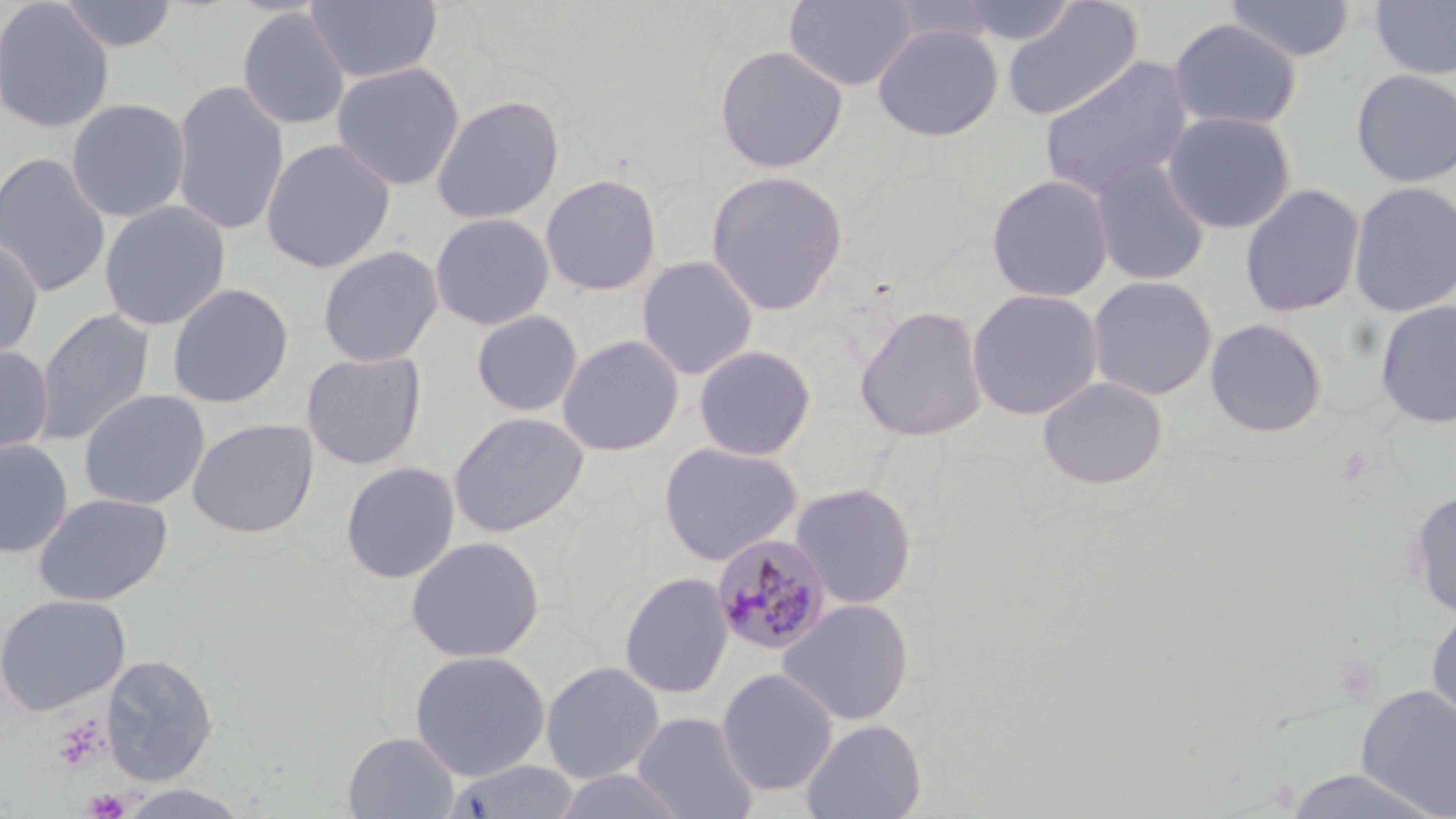
{
  "slide_level_diagnosis": "Plasmodium malariae",
  "preparation": "thin blood smear",
  "modality": "light microscopy",
  "field_of_view": "one of a larger specimen",
  "image_size": "1456×819 pixels",
  "uninfected_red_blood_cell_locations": "approximate bounding boxes as (x1, y1, x2, y2) in pixels: (0, 0, 115, 133), (56, 0, 181, 53), (305, 0, 443, 84), (784, 0, 918, 92), (952, 0, 1080, 46), (1001, 0, 1144, 121), (1223, 0, 1357, 62), (1370, 0, 1456, 79), (237, 7, 351, 131), (1167, 18, 1303, 132), (872, 23, 1004, 142), (713, 44, 849, 174), (1038, 55, 1194, 200), (331, 61, 466, 191), (1351, 68, 1456, 188), (171, 79, 290, 237), (431, 93, 565, 225), (66, 98, 191, 222), (1162, 110, 1297, 234), (260, 138, 397, 273), (0, 151, 112, 298), (1089, 156, 1212, 286), (705, 170, 850, 316), (540, 173, 663, 297), (986, 173, 1114, 303), (1348, 180, 1456, 318), (1240, 183, 1366, 318), (98, 199, 232, 331), (429, 212, 556, 331), (0, 234, 45, 363), (317, 245, 444, 367), (636, 255, 759, 379), (1087, 275, 1218, 401), (166, 282, 295, 409), (966, 287, 1104, 420), (1374, 300, 1456, 429), (853, 304, 989, 442), (34, 308, 155, 445), (470, 309, 584, 417), (1205, 318, 1328, 438), (556, 334, 685, 456), (692, 344, 818, 462), (0, 345, 54, 456), (301, 351, 427, 470), (1037, 376, 1169, 490), (77, 388, 211, 510), (447, 410, 590, 538), (186, 417, 320, 539), (0, 437, 74, 558), (658, 441, 804, 566), (340, 461, 461, 583), (789, 482, 919, 609), (1407, 488, 1456, 620), (33, 492, 173, 607), (405, 535, 546, 663), (618, 571, 734, 699), (0, 593, 131, 716), (778, 598, 914, 726), (1425, 605, 1456, 732), (409, 649, 551, 781), (100, 654, 218, 785), (540, 661, 665, 783), (716, 667, 838, 797), (1355, 684, 1456, 818), (632, 711, 758, 819), (801, 718, 926, 819), (343, 731, 460, 819), (443, 760, 581, 819), (1278, 766, 1452, 819), (115, 784, 255, 819)",
  "platelet_locations": "approximate bounding boxes as (x1, y1, x2, y2) in pixels: (51, 715, 109, 772), (83, 788, 130, 819)",
  "magnification": "1000x",
  "plasmodium_malariae_infected_red_blood_cell_locations": "approximate bounding boxes as (x1, y1, x2, y2) in pixels: (711, 534, 834, 656)",
  "stain": "May-Grünwald-Giemsa"
}